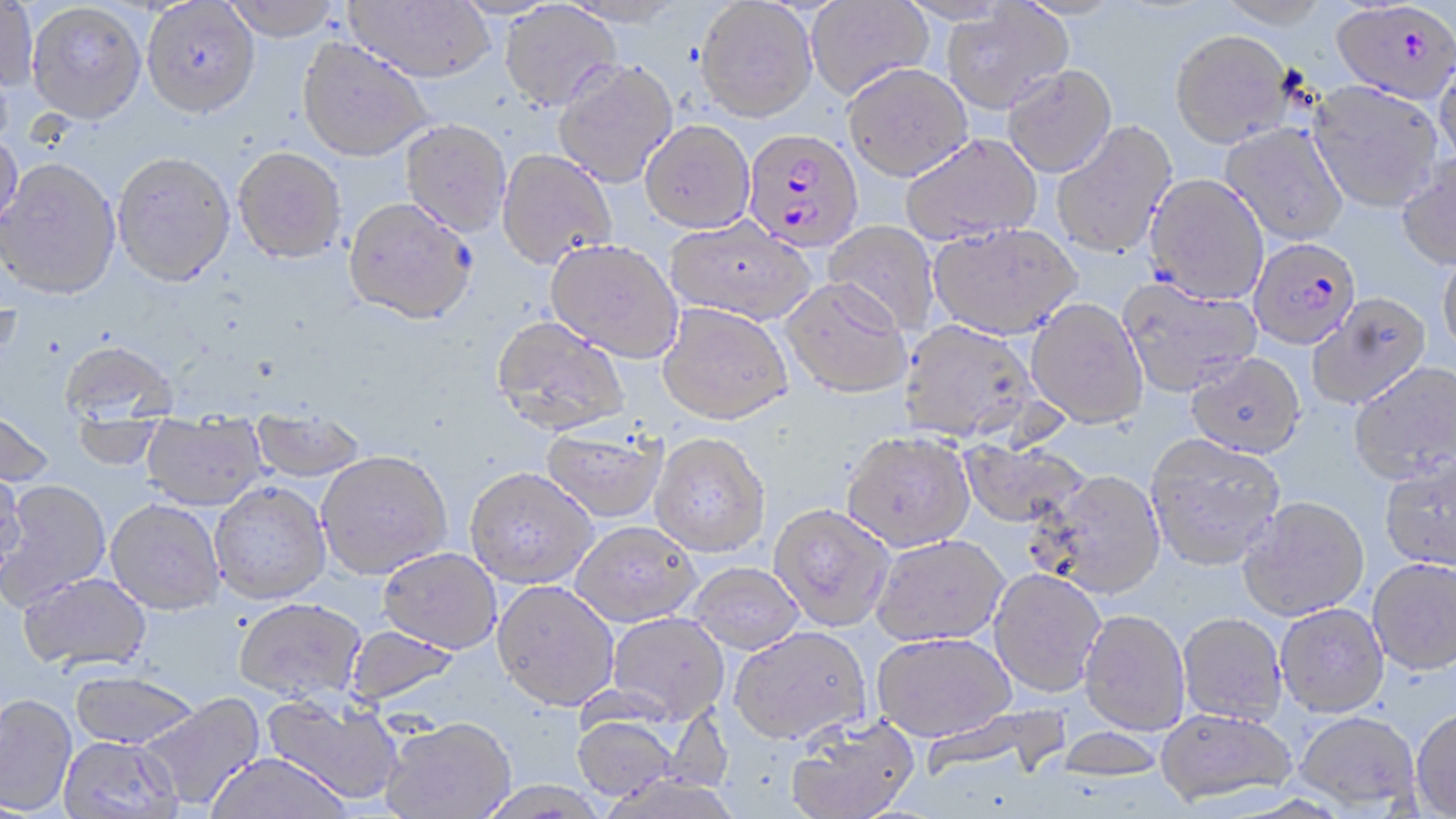
slide-level diagnosis = Plasmodium falciparum
magnification = 1000x
uninfected red blood cell locations = approximate bounding boxes as (x1,y1)-(x2,y2) corner pairs in pixels: (221,0)-(344,40), (344,0)-(494,83), (694,0)-(819,122), (805,0)-(934,101), (1217,0)-(1330,28), (0,1)-(38,95), (141,1)-(260,118), (27,2)-(147,124), (499,2)-(621,111), (940,5)-(1073,114), (1170,29)-(1294,148), (297,37)-(433,161), (1433,54)-(1456,174), (552,58)-(678,188), (842,63)-(972,181), (1001,64)-(1117,177), (1308,80)-(1444,212), (400,119)-(511,237), (640,119)-(755,233), (1051,121)-(1177,260), (1220,123)-(1349,245), (0,131)-(23,236), (899,133)-(1043,245), (233,146)-(347,263), (497,149)-(617,269), (112,150)-(235,286), (1395,153)-(1456,270), (0,157)-(121,300), (1145,173)-(1269,305), (343,195)-(477,326), (665,216)-(816,325), (822,220)-(940,335), (928,222)-(1082,339), (545,240)-(683,363), (1437,250)-(1456,359), (1117,276)-(1262,397), (781,277)-(912,398), (1307,292)-(1431,409), (1026,297)-(1148,429), (657,303)-(793,425), (490,315)-(630,436), (899,320)-(1040,443), (59,339)-(179,436), (1185,351)-(1306,458), (1348,362)-(1456,484), (0,406)-(55,488), (250,407)-(367,483), (141,412)-(268,510), (541,426)-(669,523), (842,430)-(975,552), (649,433)-(771,558), (1145,433)-(1286,570), (956,438)-(1091,529), (317,451)-(452,579), (1379,452)-(1456,572), (465,467)-(597,587), (1038,469)-(1165,598), (0,470)-(25,576), (1,479)-(110,609), (209,482)-(331,605), (1239,496)-(1371,621), (106,499)-(224,614), (768,503)-(895,631), (571,521)-(702,626), (871,534)-(1009,646), (379,547)-(502,653), (1367,558)-(1456,675), (686,562)-(805,654), (989,568)-(1105,697), (18,572)-(152,672), (492,580)-(619,710), (233,598)-(366,704), (1275,603)-(1389,716), (1079,609)-(1189,734), (606,612)-(729,723), (1178,613)-(1288,725), (343,625)-(463,708), (730,626)-(870,745), (871,632)-(1016,741), (69,669)-(200,750), (139,692)-(266,811), (0,693)-(77,815), (261,696)-(403,806), (920,703)-(1073,782), (1411,707)-(1456,818), (1155,708)-(1297,806), (1295,710)-(1420,811), (571,712)-(678,802), (785,715)-(920,819), (381,717)-(517,819), (60,735)-(181,818), (205,753)-(351,818), (476,781)-(610,819)
stain = May-Grünwald-Giemsa
preparation = thin blood smear
modality = optical microscopy
field of view = one of a larger specimen
image size = 1456×819 pixels
Plasmodium falciparum-infected red blood cell locations = approximate bounding boxes as (x1,y1)-(x2,y2) corner pairs in pixels: (1330,2)-(1456,104), (743,128)-(864,252), (1248,237)-(1361,349)